Describe the morphology of the erythrocytes.
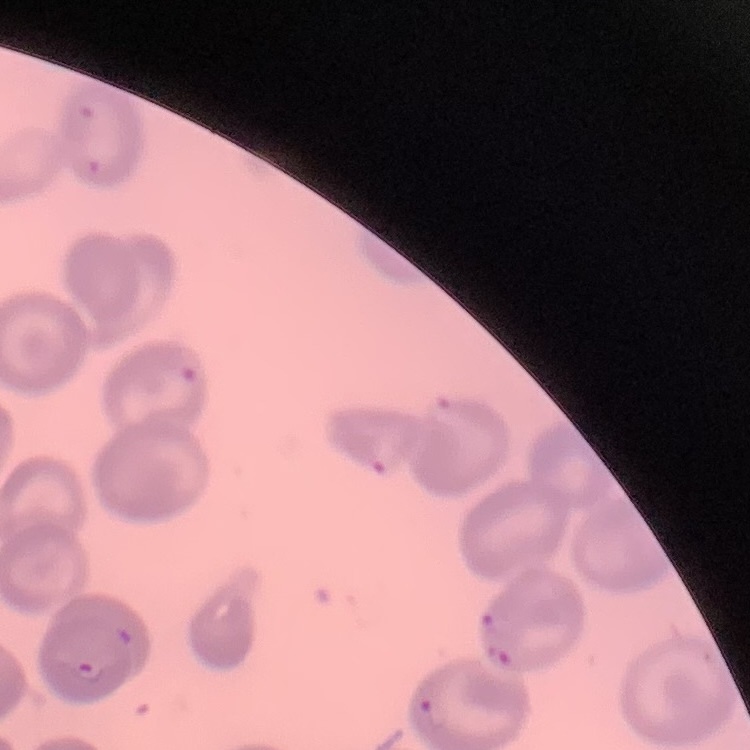

No rouleaux formation.

Thin blood smear. One tile cut from a larger photomicrograph. Stained with either Field's or Giemsa.